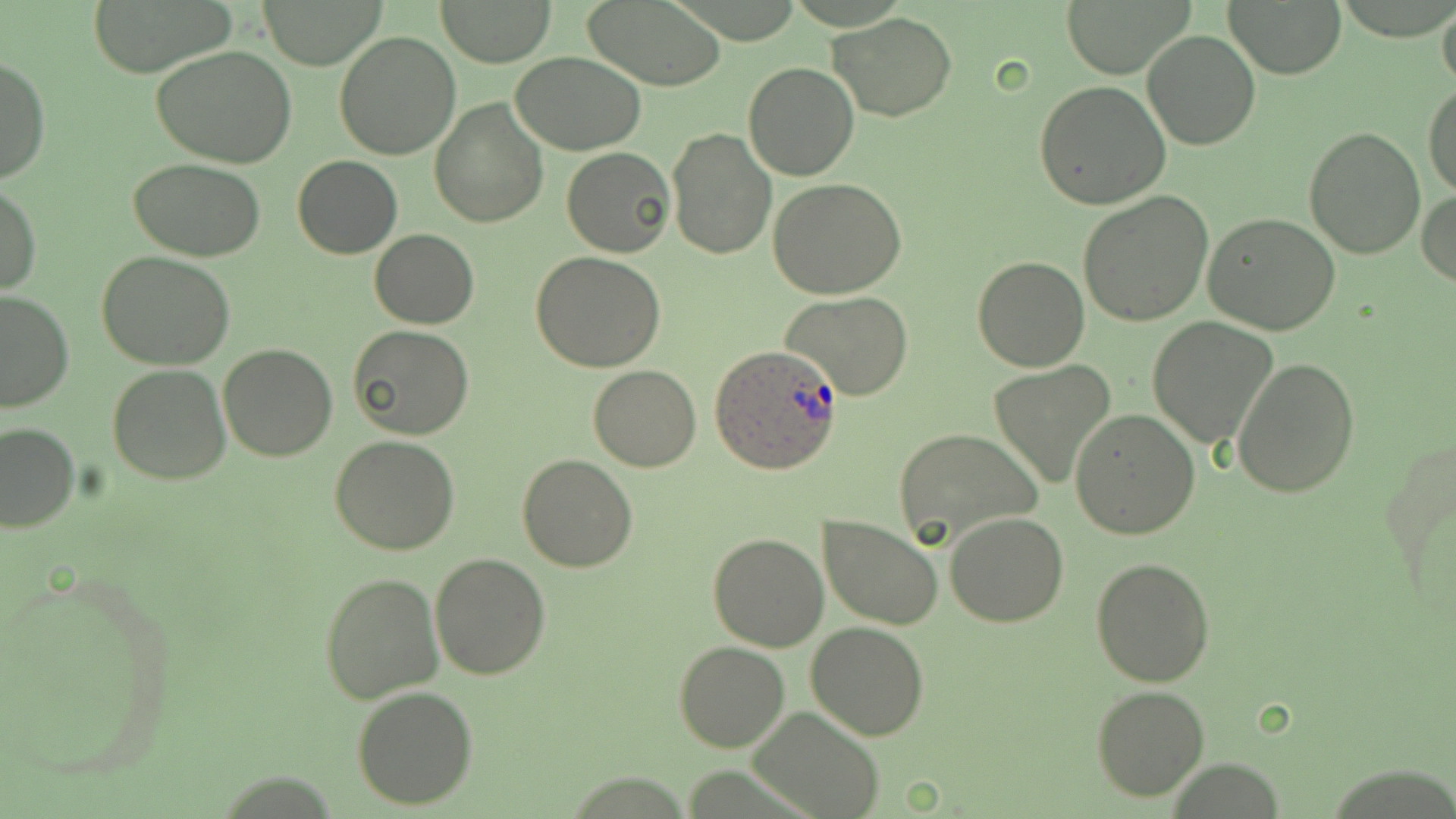

Summary:
  - Coordinate format: approximate bounding boxes as (x1,y1)-(x2,y2) corner pairs in pixels
  - Plasmodium ovale-infected red blood cell locations: (710,345)-(842,472)
  - Uninfected red blood cell locations: (435,0)-(557,67), (577,0)-(729,89), (1058,0)-(1193,79), (1226,0)-(1345,79), (262,1)-(383,69), (1437,1)-(1456,97), (85,2)-(236,75), (1170,8)-(1336,104), (830,12)-(957,121), (1141,30)-(1261,150), (332,31)-(460,161), (153,46)-(299,169), (511,52)-(646,156), (1,57)-(51,186), (742,62)-(860,182), (1034,80)-(1170,209), (1423,80)-(1456,199), (429,96)-(548,227), (1304,126)-(1425,259), (665,127)-(778,263), (562,147)-(675,258), (293,156)-(401,259), (129,158)-(265,262), (767,179)-(908,299), (1,184)-(41,296), (1078,189)-(1214,325), (1417,189)-(1456,290), (1203,213)-(1343,336), (369,228)-(478,330), (97,251)-(236,370), (532,253)-(665,371), (972,254)-(1090,372), (0,290)-(74,413), (779,292)-(914,402), (1147,317)-(1277,448), (348,325)-(475,441), (218,343)-(339,461), (1232,357)-(1360,498), (106,362)-(232,484), (987,362)-(1115,487), (589,364)-(702,472), (1071,409)-(1200,538), (0,422)-(80,532), (892,427)-(1042,549), (329,436)-(461,555), (517,453)-(637,573), (946,511)-(1069,626), (820,514)-(943,629), (708,533)-(828,652), (429,554)-(551,680), (1090,557)-(1216,688), (319,571)-(444,704), (805,619)-(930,739), (674,641)-(790,752), (352,685)-(477,810), (1091,685)-(1211,802), (752,706)-(882,818)
  - Slide-level diagnosis: Plasmodium ovale
  - Magnification: 1000x
  - Preparation: thin blood film
  - Modality: optical microscopy
  - Field of view: one of a larger specimen
  - Stain: May-Grünwald-Giemsa
  - Image size: 1456×819 pixels